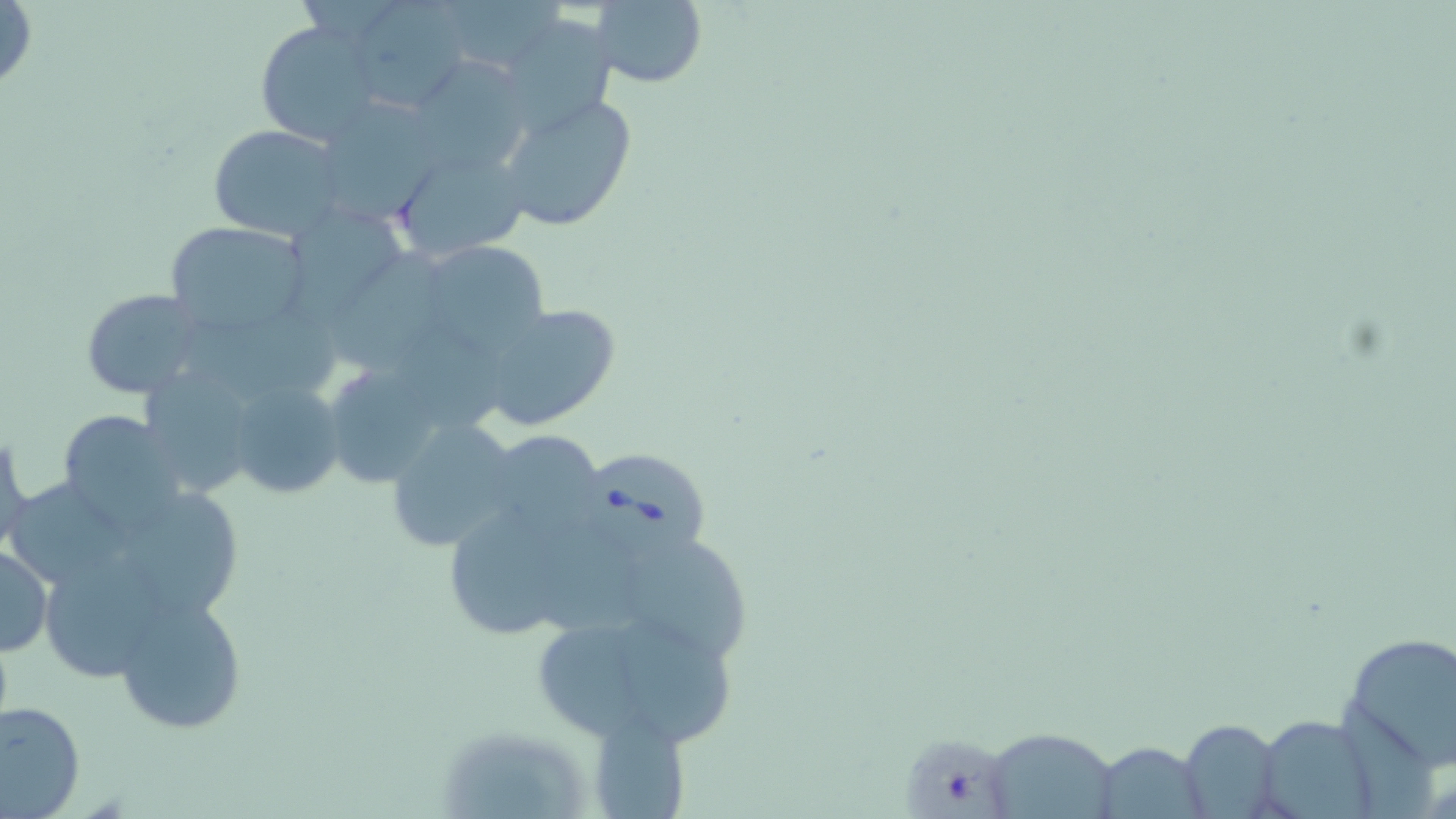

Summary:
  - Coordinate format: approximate bounding boxes as (x1, y1, x2, y2) in pixels
  - Babesia divergens-infected red blood cell locations: (579, 451, 708, 555)
  - Uninfected red blood cell locations: (591, 0, 709, 89), (0, 1, 38, 96), (343, 2, 473, 114), (497, 13, 617, 132), (256, 20, 377, 148), (228, 35, 366, 236), (419, 50, 531, 163), (497, 91, 640, 233), (314, 97, 447, 226), (208, 126, 347, 240), (389, 141, 532, 266), (298, 206, 409, 316), (161, 220, 309, 338), (413, 240, 553, 355), (332, 244, 449, 377), (79, 289, 209, 400), (184, 301, 343, 401), (473, 302, 624, 433), (319, 360, 453, 492), (148, 377, 255, 498), (224, 379, 343, 500), (55, 407, 187, 528), (385, 417, 522, 555), (0, 422, 31, 554), (482, 430, 605, 541), (11, 477, 131, 588), (127, 495, 255, 628), (440, 498, 597, 638), (0, 542, 52, 658), (634, 545, 759, 660), (45, 561, 176, 674), (111, 592, 251, 737), (530, 598, 739, 753), (1338, 631, 1456, 771), (1, 700, 86, 817), (585, 709, 691, 819), (1254, 713, 1380, 819), (1177, 720, 1283, 818), (983, 728, 1119, 819), (1095, 740, 1209, 817)
  - Slide-level diagnosis: Babesia divergens
  - Preparation: thin blood smear
  - Image size: 1456×819 pixels
  - Field of view: one of a larger specimen
  - Magnification: 1000x
  - Stain: May-Grünwald-Giemsa
  - Modality: light microscopy